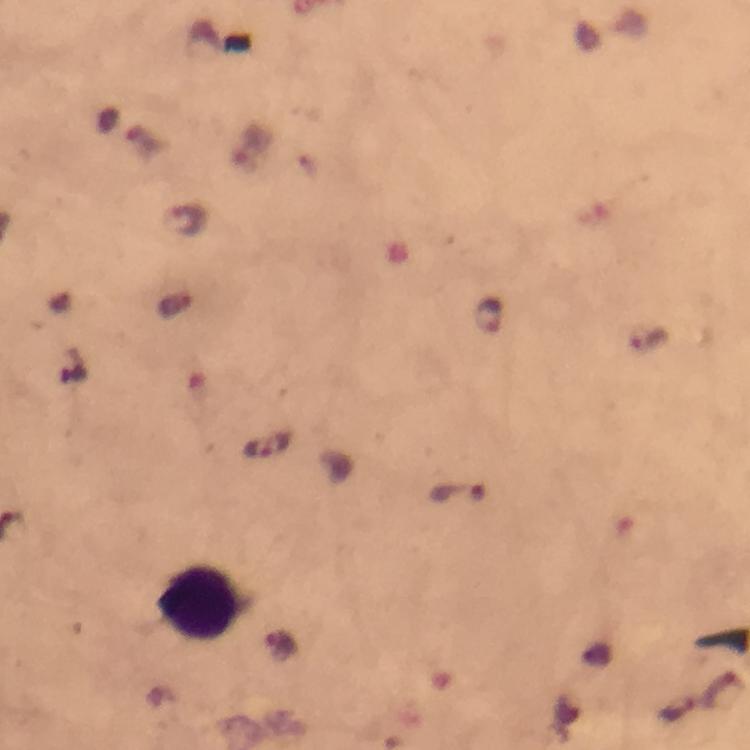

leukocyte locations = approximate object centers, in pixels from the top-left corner: (x=201, y=606)
preparation = thick blood smear
cropped from = a single field of view
magnification = 100x
context = from a malaria diagnostic workup
stain = Giemsa
malaria parasite locations = approximate object centers, in pixels from the top-left corner: (x=185, y=218), (x=489, y=315), (x=646, y=337), (x=266, y=447), (x=458, y=494), (x=280, y=646), (x=723, y=690), (x=677, y=710)
image size = 750×750 pixels
immersion oil = used
capture = smartphone mounted on the microscope